Identify the cell.
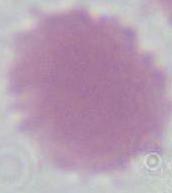

An erythrocyte.

Micrograph. 1000x magnification.